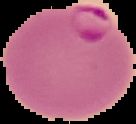 The area outside the segmented cell region is set to black. Image is 136×124 pixels. Malaria status: parasitized. From a thin blood smear.